Identify the blood parasite species.
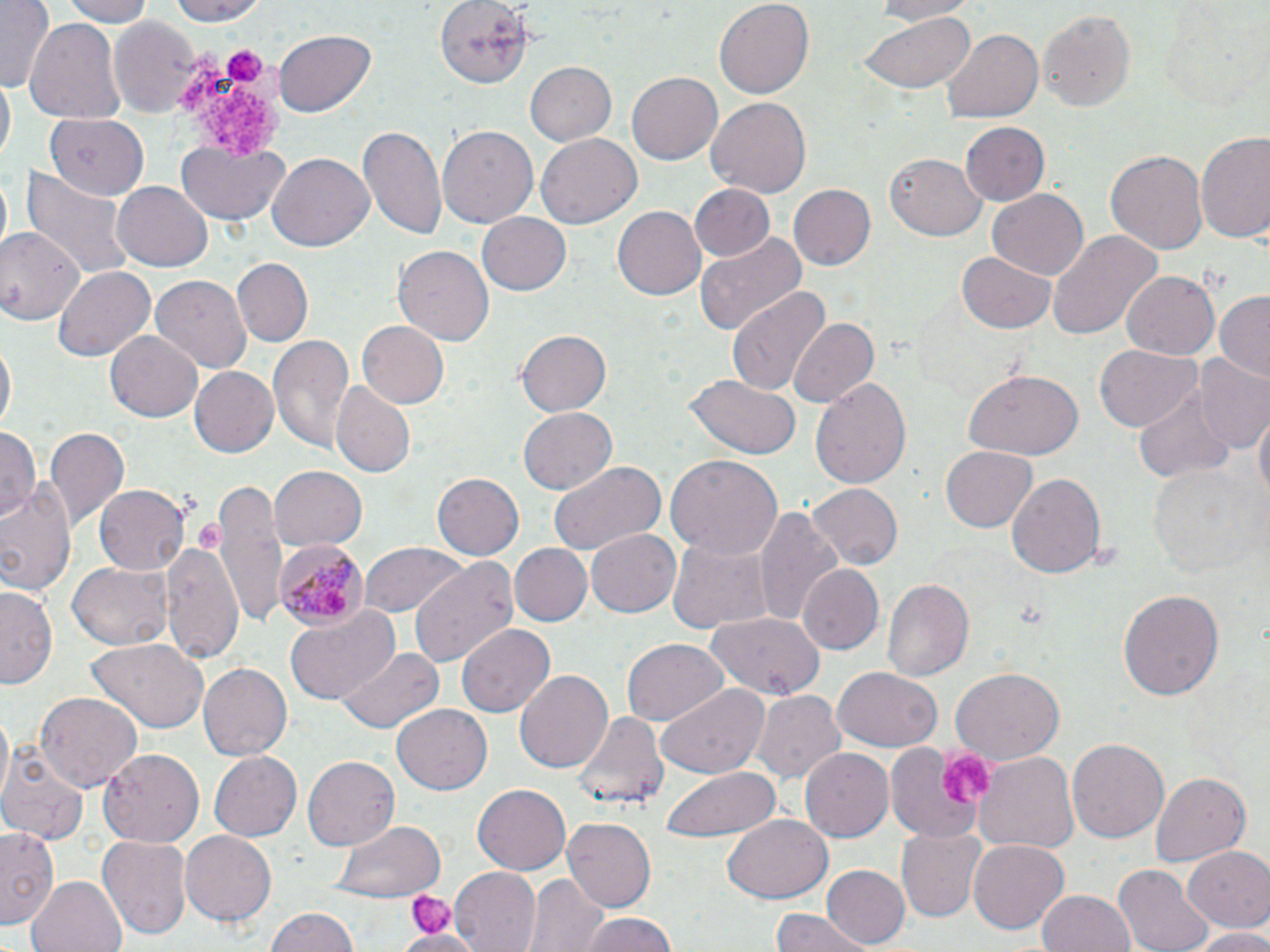

Plasmodium malariae.

Approximate bounding boxes as named x1/y1/x2/y2 corners in pixels. Platelet locations: (x1=177, y1=46, x2=289, y2=161), (x1=224, y1=48, x2=264, y2=84), (x1=939, y1=744, x2=997, y2=811), (x1=409, y1=891, x2=455, y2=936). Plasmodium malariae-infected red blood cell locations: (x1=274, y1=538, x2=367, y2=629). Uninfected red blood cell locations: (x1=1, y1=0, x2=55, y2=91), (x1=57, y1=0, x2=157, y2=25), (x1=158, y1=0, x2=275, y2=25), (x1=434, y1=0, x2=534, y2=88), (x1=867, y1=0, x2=984, y2=24), (x1=713, y1=1, x2=815, y2=100), (x1=1038, y1=7, x2=1136, y2=114), (x1=106, y1=14, x2=202, y2=120), (x1=859, y1=14, x2=974, y2=96), (x1=24, y1=16, x2=126, y2=127), (x1=941, y1=29, x2=1042, y2=123), (x1=273, y1=30, x2=375, y2=118), (x1=522, y1=61, x2=616, y2=148), (x1=628, y1=72, x2=722, y2=164), (x1=1, y1=78, x2=15, y2=168), (x1=706, y1=96, x2=813, y2=196), (x1=45, y1=115, x2=150, y2=199), (x1=962, y1=122, x2=1049, y2=206), (x1=436, y1=124, x2=537, y2=227), (x1=358, y1=125, x2=447, y2=240), (x1=535, y1=132, x2=641, y2=228), (x1=1196, y1=133, x2=1270, y2=246), (x1=175, y1=138, x2=287, y2=226), (x1=1105, y1=148, x2=1208, y2=257), (x1=886, y1=150, x2=987, y2=241), (x1=267, y1=154, x2=374, y2=253), (x1=20, y1=168, x2=132, y2=282), (x1=113, y1=181, x2=213, y2=271), (x1=690, y1=184, x2=774, y2=263), (x1=787, y1=184, x2=877, y2=271), (x1=987, y1=190, x2=1088, y2=280), (x1=612, y1=204, x2=706, y2=297), (x1=478, y1=213, x2=572, y2=296), (x1=0, y1=224, x2=85, y2=327), (x1=1047, y1=230, x2=1161, y2=339), (x1=695, y1=232, x2=807, y2=339), (x1=392, y1=246, x2=498, y2=347), (x1=958, y1=250, x2=1057, y2=332), (x1=234, y1=259, x2=313, y2=345), (x1=52, y1=266, x2=155, y2=364), (x1=1120, y1=270, x2=1220, y2=361), (x1=150, y1=275, x2=252, y2=374), (x1=726, y1=285, x2=830, y2=396), (x1=1212, y1=291, x2=1270, y2=382), (x1=788, y1=316, x2=880, y2=409), (x1=356, y1=320, x2=449, y2=409), (x1=105, y1=330, x2=204, y2=422), (x1=514, y1=330, x2=610, y2=417), (x1=269, y1=334, x2=356, y2=454), (x1=0, y1=342, x2=16, y2=437), (x1=1094, y1=344, x2=1199, y2=433), (x1=1194, y1=356, x2=1270, y2=453), (x1=187, y1=366, x2=277, y2=457), (x1=964, y1=369, x2=1083, y2=459), (x1=684, y1=375, x2=801, y2=460), (x1=810, y1=377, x2=911, y2=490), (x1=330, y1=380, x2=415, y2=477), (x1=1133, y1=382, x2=1233, y2=483), (x1=1253, y1=406, x2=1268, y2=508), (x1=518, y1=408, x2=615, y2=494), (x1=43, y1=424, x2=130, y2=528), (x1=0, y1=426, x2=39, y2=523), (x1=939, y1=445, x2=1039, y2=533), (x1=665, y1=453, x2=784, y2=561), (x1=549, y1=460, x2=665, y2=556), (x1=1148, y1=460, x2=1257, y2=577), (x1=270, y1=466, x2=367, y2=551), (x1=433, y1=472, x2=527, y2=561), (x1=1007, y1=473, x2=1107, y2=577), (x1=0, y1=477, x2=79, y2=599), (x1=214, y1=479, x2=292, y2=626), (x1=95, y1=483, x2=191, y2=575), (x1=806, y1=484, x2=904, y2=570), (x1=755, y1=506, x2=847, y2=633), (x1=587, y1=528, x2=681, y2=617), (x1=666, y1=531, x2=775, y2=638), (x1=162, y1=540, x2=242, y2=665), (x1=357, y1=543, x2=469, y2=622), (x1=507, y1=543, x2=591, y2=627), (x1=409, y1=558, x2=519, y2=666), (x1=68, y1=562, x2=171, y2=649), (x1=800, y1=564, x2=883, y2=656), (x1=880, y1=578, x2=973, y2=685), (x1=1, y1=584, x2=59, y2=688), (x1=1117, y1=589, x2=1224, y2=703), (x1=285, y1=605, x2=402, y2=707), (x1=705, y1=610, x2=825, y2=699), (x1=458, y1=624, x2=555, y2=717), (x1=85, y1=638, x2=211, y2=734), (x1=621, y1=638, x2=728, y2=727), (x1=338, y1=647, x2=444, y2=734), (x1=198, y1=662, x2=292, y2=761), (x1=831, y1=666, x2=944, y2=752), (x1=950, y1=666, x2=1063, y2=764), (x1=515, y1=669, x2=612, y2=776), (x1=654, y1=682, x2=771, y2=776), (x1=754, y1=691, x2=847, y2=789), (x1=35, y1=693, x2=142, y2=791), (x1=391, y1=705, x2=493, y2=794), (x1=570, y1=711, x2=669, y2=810), (x1=1068, y1=738, x2=1169, y2=845), (x1=884, y1=740, x2=994, y2=842), (x1=0, y1=747, x2=89, y2=846), (x1=801, y1=748, x2=894, y2=842), (x1=101, y1=749, x2=204, y2=845), (x1=209, y1=750, x2=302, y2=842), (x1=973, y1=753, x2=1079, y2=858), (x1=303, y1=755, x2=399, y2=851), (x1=661, y1=767, x2=781, y2=843), (x1=1151, y1=771, x2=1250, y2=867), (x1=472, y1=782, x2=572, y2=874), (x1=724, y1=815, x2=834, y2=903), (x1=563, y1=817, x2=656, y2=913), (x1=332, y1=819, x2=447, y2=901), (x1=0, y1=826, x2=59, y2=925), (x1=897, y1=829, x2=986, y2=920), (x1=180, y1=831, x2=276, y2=926), (x1=98, y1=834, x2=193, y2=941), (x1=968, y1=838, x2=1070, y2=935), (x1=1184, y1=846, x2=1270, y2=933), (x1=821, y1=864, x2=908, y2=949), (x1=449, y1=865, x2=543, y2=952), (x1=1118, y1=865, x2=1214, y2=952), (x1=524, y1=873, x2=605, y2=952), (x1=27, y1=875, x2=126, y2=952), (x1=1036, y1=889, x2=1136, y2=952), (x1=266, y1=908, x2=358, y2=952), (x1=768, y1=912, x2=869, y2=952), (x1=574, y1=914, x2=682, y2=952), (x1=1186, y1=927, x2=1270, y2=952), (x1=398, y1=930, x2=482, y2=952). Optical microscopy. May-Grünwald-Giemsa stain. 1000x magnification. Single field of view. Thin blood smear. Image is 1270×952 pixels.